Report the malaria status of this cell.
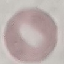

It is uninfected.

capture = smartphone through the microscope eyepiece
preparation = thin smear
image type = cell patch, automatically extracted from a larger field of view and resized to 64 × 64 pixels
stain = Giemsa